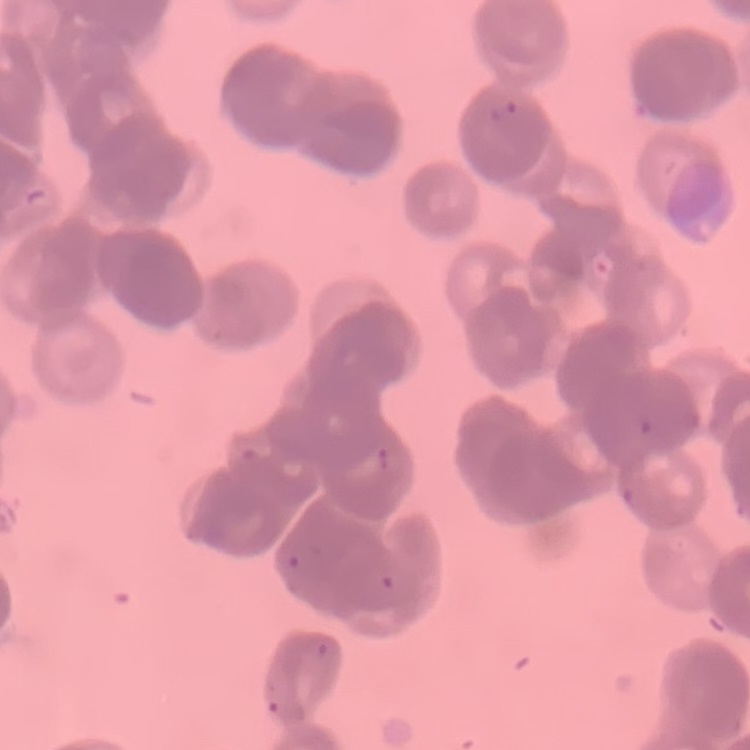
red blood cell morphology = rouleaux formation
image type = square crop of a larger photomicrograph
stain = Field's or Giemsa
preparation = thin peripheral smear